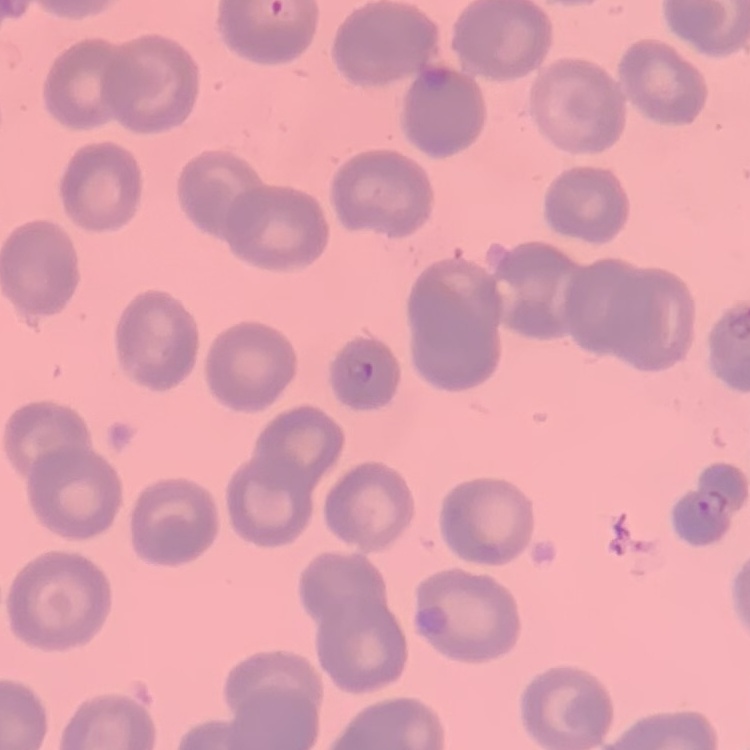
The erythrocytes show no rouleaux formation. Thin blood film. Square crop of a larger photomicrograph. Stained with either Field's or Giemsa.